Report the malaria status of this cell.
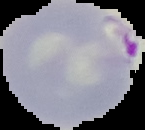

It is parasitized.

preparation = thin blood smear
image type = cell region segmented out of the field of view; surrounding area masked to black
image size = 145×130 pixels